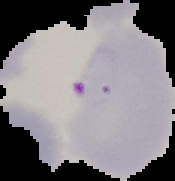

From a thin blood smear. Malaria status: parasitized. Image is 175×181 pixels. Segmented cell region on a black background.